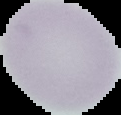 From a thin blood smear. Segmented cell region on a black background. Result: no malaria parasites detected. Image is 121×115 pixels.